Locate every Plasmodium parasite.
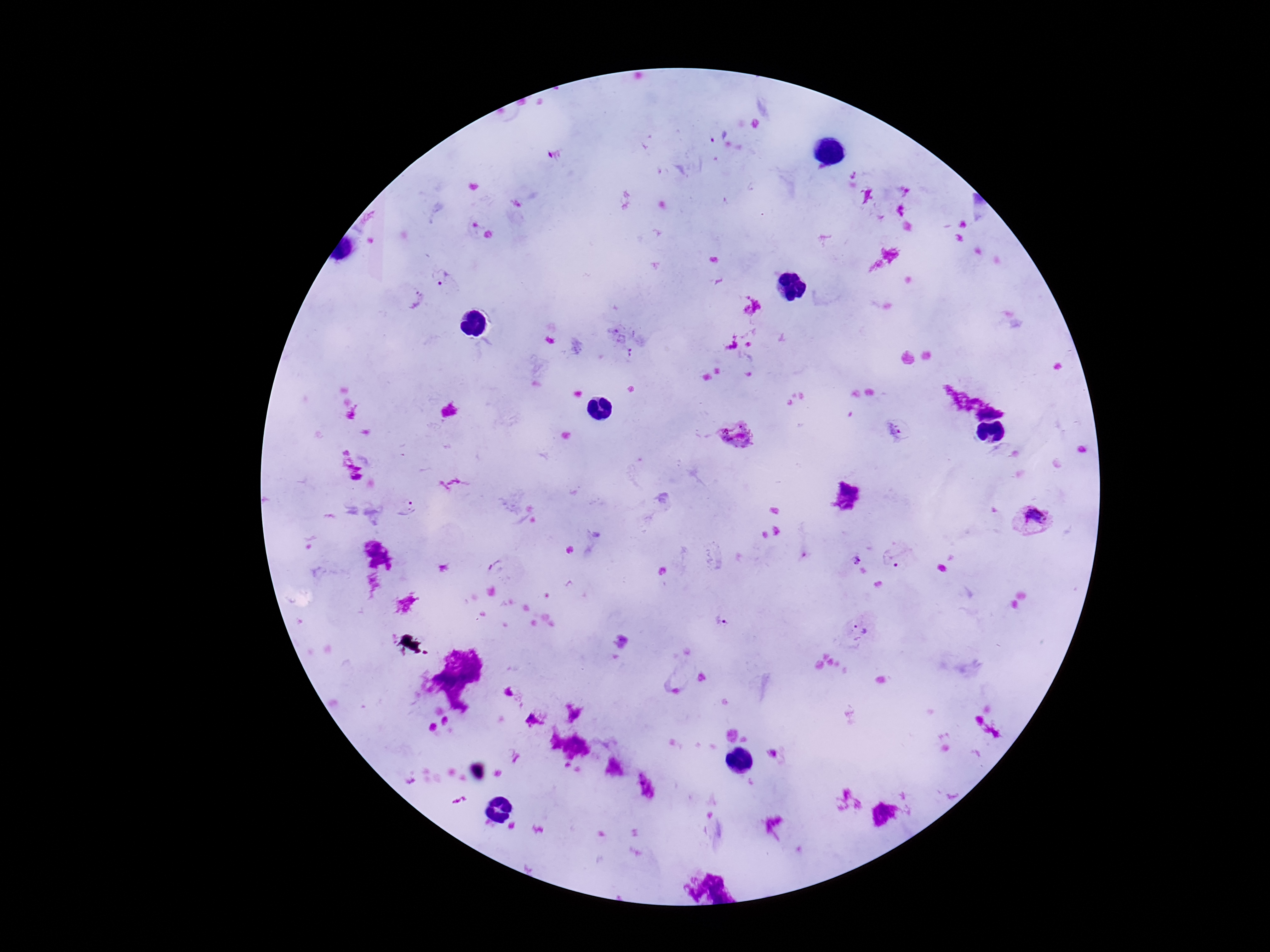
Approximate centers as (x, y) in pixels.
Plasmodium parasites: (716, 133), (445, 280), (418, 293), (630, 354), (897, 432), (737, 434), (406, 509), (1030, 519), (854, 557), (897, 565), (721, 622), (863, 626).

One field from this slide. 100x magnification. Giemsa stain. Image is 1270×952 pixels. Patient malaria status: positive. Thick peripheral-blood smear. Photographed through the microscope eyepiece with a smartphone camera.